Outline each Plasmodium falciparum-infected red blood cell.
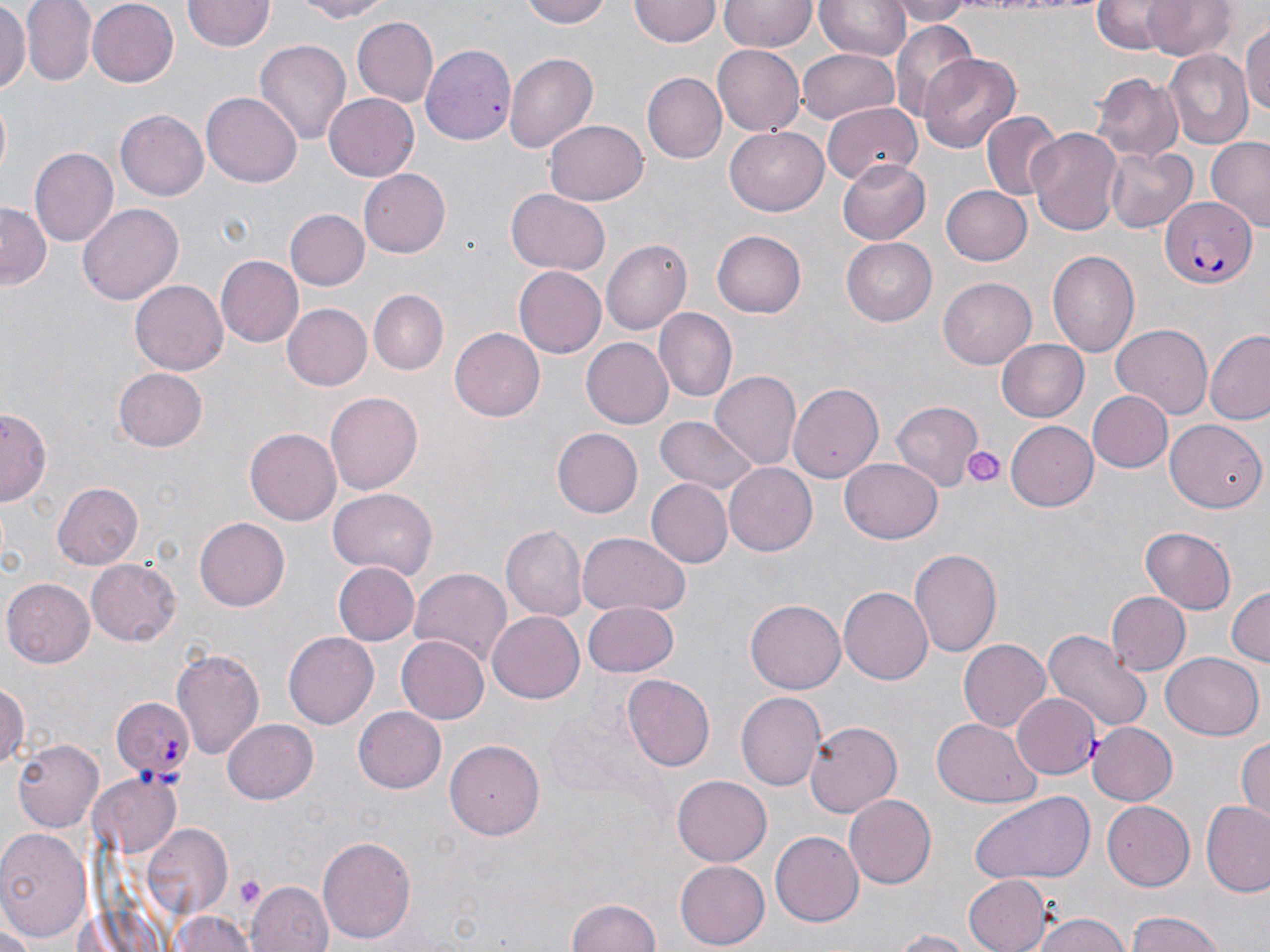
Approximate bounding boxes as [x1, y1, x2, y2] in pixels.
Plasmodium falciparum-infected red blood cells: [1161, 197, 1256, 288], [1011, 692, 1102, 779], [115, 696, 196, 781].

slide-level diagnosis = Plasmodium falciparum
field of view = one of a larger specimen
preparation = thin blood film
stain = May-Grünwald-Giemsa
platelet locations = approximate bounding boxes as [x1, y1, x2, y2] in pixels: [962, 444, 1006, 489], [234, 873, 267, 908]
modality = light microscopy
magnification = 1000x
image size = 1270×952 pixels
uninfected red blood cell locations = approximate bounding boxes as [x1, y1, x2, y2] in pixels: [0, 0, 30, 91], [21, 0, 96, 87], [86, 0, 181, 87], [287, 0, 398, 22], [522, 0, 613, 27], [816, 0, 909, 61], [888, 0, 974, 24], [1090, 0, 1173, 52], [1144, 0, 1236, 61], [184, 1, 273, 53], [629, 1, 720, 47], [719, 1, 816, 53], [351, 18, 440, 107], [890, 23, 980, 120], [1243, 23, 1270, 121], [255, 40, 351, 147], [420, 41, 516, 142], [712, 46, 805, 136], [798, 47, 899, 125], [1163, 49, 1254, 148], [919, 51, 1021, 152], [504, 53, 597, 156], [645, 72, 728, 164], [1091, 73, 1182, 161], [323, 92, 419, 180], [202, 94, 302, 186], [825, 97, 927, 180], [117, 110, 208, 201], [981, 111, 1062, 201], [546, 118, 648, 205], [725, 128, 827, 215], [1028, 128, 1122, 237], [1205, 138, 1270, 232], [29, 146, 118, 249], [1104, 146, 1197, 235], [836, 158, 931, 244], [357, 169, 450, 258], [942, 185, 1034, 267], [505, 189, 610, 276], [79, 202, 183, 304], [0, 203, 48, 287], [283, 209, 368, 291], [712, 231, 806, 317], [841, 237, 940, 326], [602, 240, 691, 333], [1047, 249, 1140, 357], [216, 255, 304, 346], [514, 266, 606, 358], [940, 276, 1036, 369], [132, 280, 228, 377], [367, 289, 448, 375], [280, 303, 371, 391], [652, 309, 736, 402], [1111, 323, 1214, 418], [451, 327, 545, 420], [1206, 331, 1270, 424], [582, 337, 672, 428], [995, 338, 1088, 423], [113, 368, 209, 451], [710, 371, 800, 472], [788, 383, 885, 482], [325, 390, 422, 492], [1089, 391, 1173, 472], [893, 401, 986, 490], [2, 408, 50, 508], [658, 417, 757, 496], [1165, 418, 1264, 510], [1006, 421, 1098, 511], [550, 427, 641, 516], [245, 428, 341, 526], [841, 456, 942, 543], [723, 462, 816, 555], [646, 477, 733, 568], [53, 481, 143, 569], [326, 488, 438, 579], [195, 516, 289, 610], [502, 525, 587, 620], [1140, 527, 1237, 613], [577, 532, 690, 617], [909, 548, 1002, 654], [86, 558, 182, 645], [331, 561, 418, 647], [411, 568, 511, 669], [4, 579, 96, 668], [837, 585, 932, 681], [1226, 585, 1269, 670], [1106, 592, 1191, 675], [748, 599, 845, 695], [582, 601, 679, 676], [486, 610, 585, 703], [1043, 629, 1153, 733], [282, 632, 377, 730], [395, 635, 492, 724], [958, 638, 1052, 733], [170, 645, 266, 761], [1163, 652, 1262, 740], [624, 673, 717, 770], [0, 681, 28, 774], [738, 691, 826, 791], [354, 707, 447, 793], [224, 718, 319, 805], [932, 718, 1042, 808], [805, 719, 902, 818], [1088, 721, 1178, 805], [1234, 734, 1270, 822], [11, 738, 102, 832], [447, 739, 545, 841], [92, 774, 180, 855], [672, 775, 770, 866], [968, 791, 1094, 884], [845, 795, 935, 886], [1102, 801, 1196, 891], [1201, 801, 1270, 895], [0, 824, 94, 946], [142, 825, 234, 922], [771, 829, 864, 925], [317, 836, 418, 944], [673, 859, 769, 949], [964, 874, 1051, 952], [249, 881, 333, 952], [567, 896, 662, 952], [165, 909, 258, 952], [1125, 910, 1228, 952], [1030, 911, 1132, 952], [886, 929, 977, 951]